Assess for malaria.
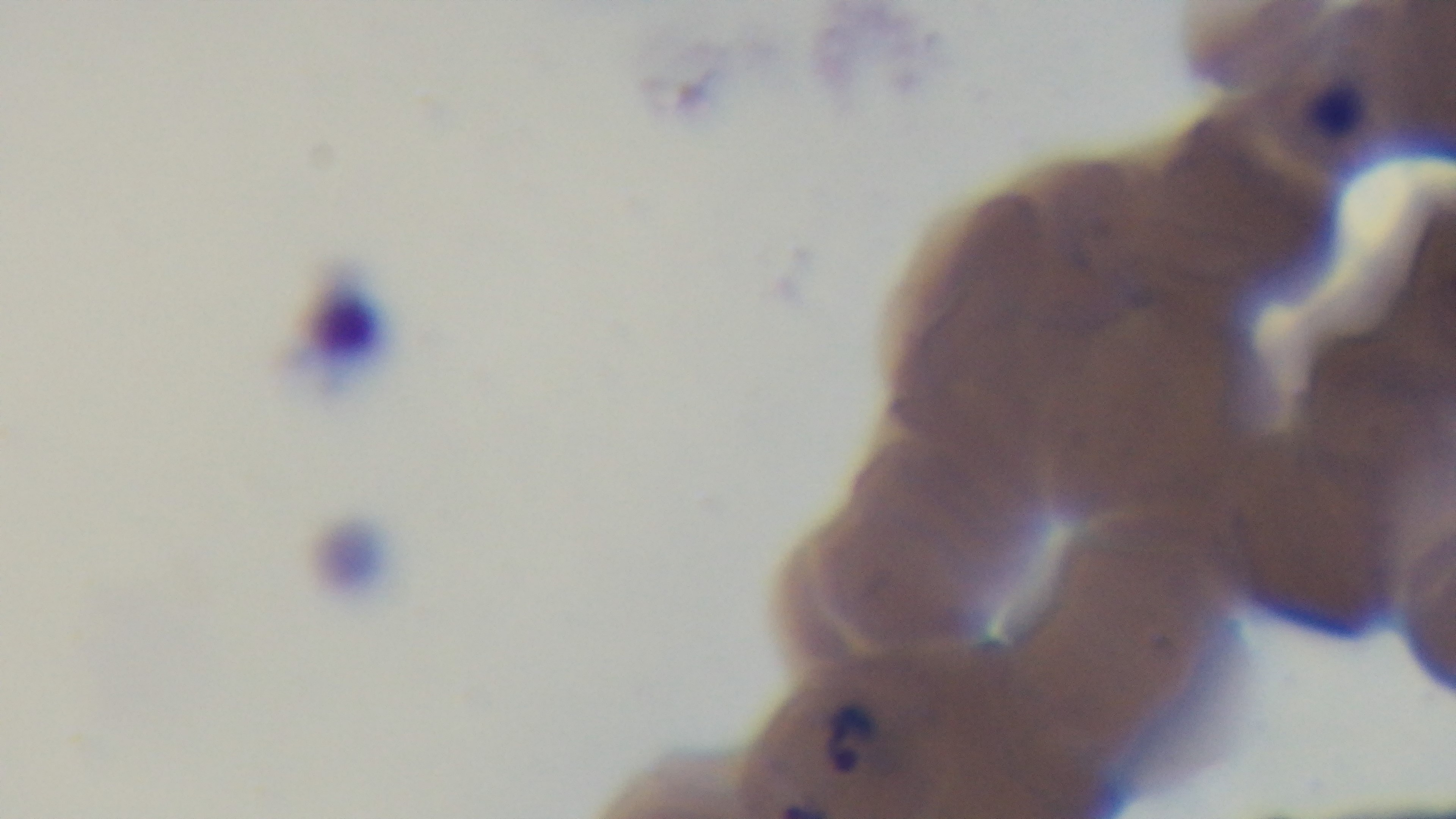
It is infected.

Mounted 4K digital camera. Photomicrograph. 100x oil-immersion objective. Giemsa-stained. Single field of view. Preparation: thin blood film.